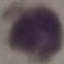
{
  "result": "negative for malaria parasites",
  "image_type": "automatically extracted cell patch, resized to 64 × 64 pixels",
  "preparation": "thin blood smear",
  "stain": "Giemsa",
  "capture": "smartphone through the microscope eyepiece"
}